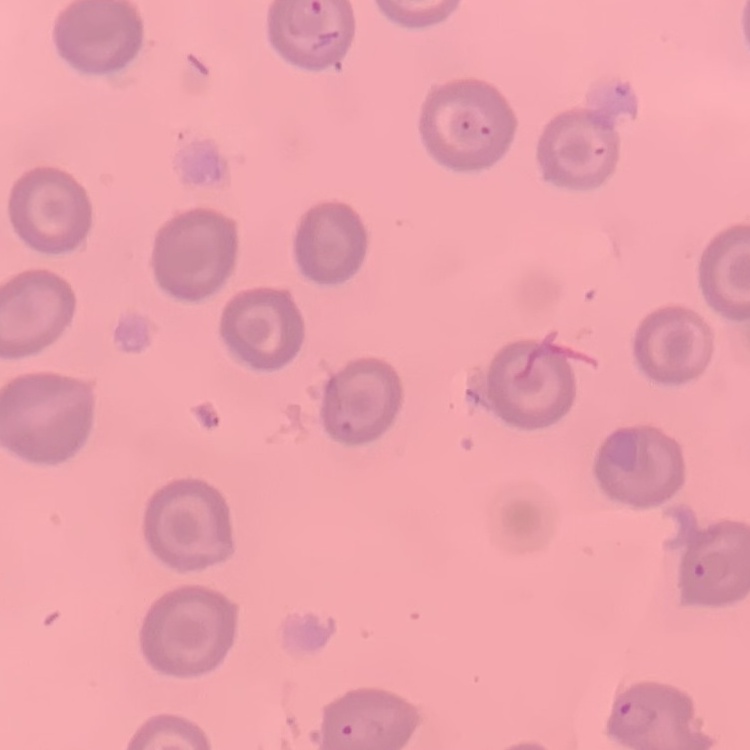

Summary:
  - Red blood cell morphology: no rouleaux formation
  - Stain: Field's or Giemsa
  - Image type: one tile cut from a larger photomicrograph
  - Preparation: thin blood smear